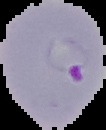

preparation = thin blood film
malaria status = parasitized
image size = 106×130 pixels
image type = segmented cell region on a black background